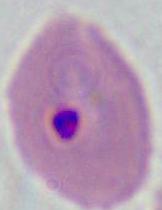
modality = micrograph
identification = Plasmodium
magnification = 400x or 1000x